Report the malaria status of this cell.
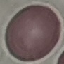

It is uninfected.

Photographed with a smartphone camera at the microscope eyepiece. Thin blood film. Automatically extracted cell patch, resized to 64 × 64 pixels. Giemsa stain.